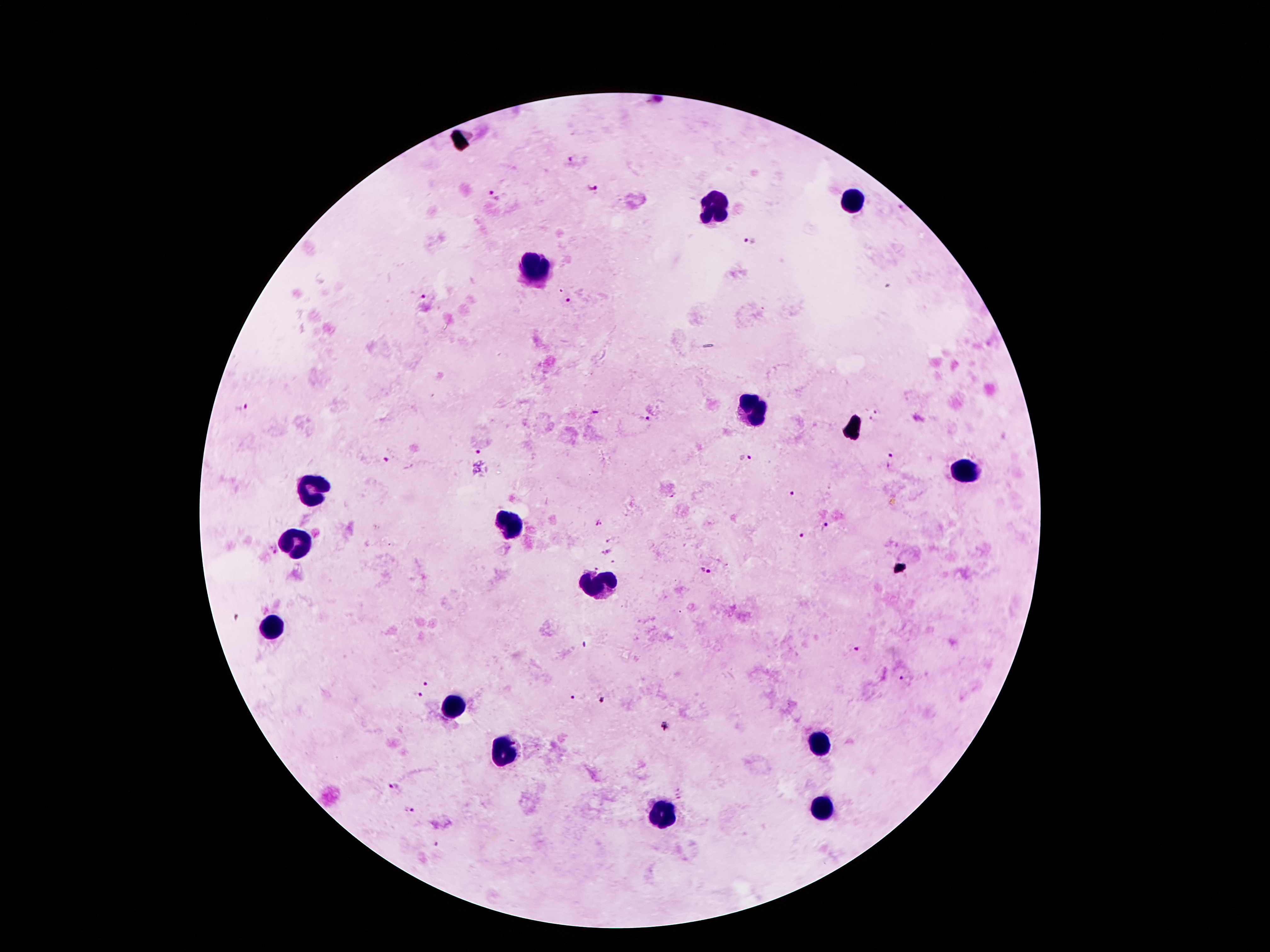 Approximate centers as (x, y) in pixels. Leukocyte locations: (855, 201), (713, 207), (538, 267), (754, 405), (963, 471), (314, 494), (512, 527), (298, 548), (594, 586), (273, 628), (454, 705), (818, 743), (504, 748), (823, 809), (662, 814). Plasmodium parasite locations: (572, 160), (593, 189), (491, 195), (749, 243), (422, 298), (567, 300), (242, 409), (880, 409), (644, 418), (871, 421), (479, 450), (746, 457), (891, 460), (385, 461), (789, 493), (599, 525), (826, 526), (804, 537), (609, 539), (272, 548), (607, 552), (613, 563), (705, 571), (237, 617), (584, 644), (854, 647), (904, 678), (427, 683), (419, 696), (571, 697), (603, 699), (392, 786), (409, 810), (437, 845). One field from this slide. Thick blood smear. Giemsa-stained preparation. 100x magnification. Image is 1270×952 pixels. Patient malaria status: positive for Plasmodium falciparum. Smartphone photograph taken through the microscope eyepiece.